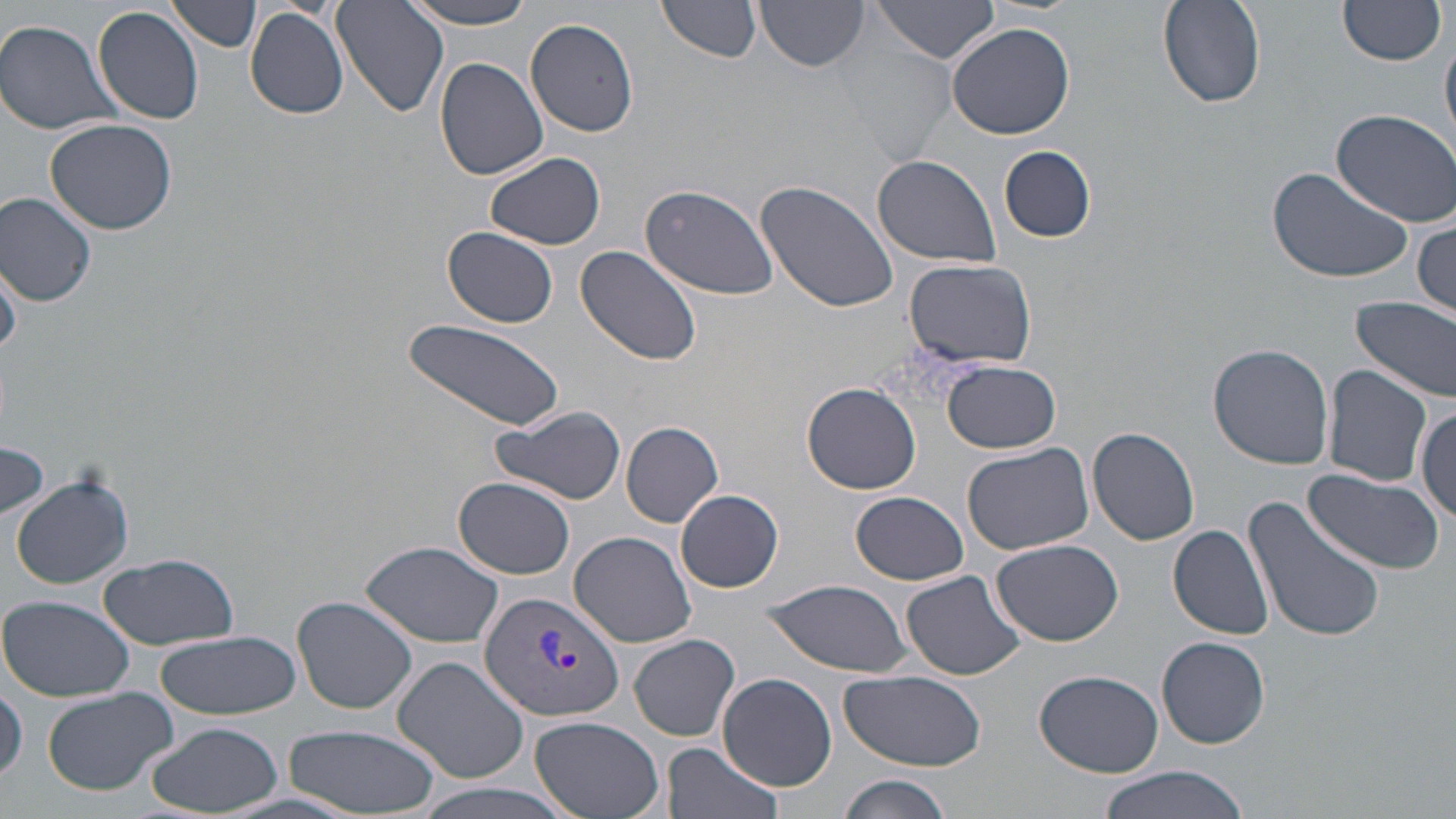

slide-level diagnosis = Plasmodium vivax
stain = May-Grünwald-Giemsa
field of view = single
preparation = thin blood film
magnification = 1000x
modality = optical microscopy
image size = 1456×819 pixels
uninfected red blood cell locations = approximate bounding boxes as [x1, y1, x2, y2] in pixels: [166, 0, 262, 52], [333, 0, 447, 117], [396, 0, 545, 28], [1156, 0, 1264, 108], [659, 1, 761, 63], [756, 1, 870, 74], [868, 1, 1002, 63], [1338, 2, 1446, 67], [94, 7, 207, 124], [244, 8, 350, 120], [524, 16, 639, 136], [0, 21, 124, 134], [946, 23, 1075, 140], [1441, 33, 1455, 149], [841, 48, 958, 163], [435, 57, 548, 180], [1329, 107, 1456, 226], [44, 118, 178, 237], [999, 146, 1097, 243], [484, 152, 607, 250], [873, 156, 1003, 269], [1265, 166, 1416, 285], [756, 181, 897, 316], [640, 182, 779, 302], [0, 193, 99, 307], [1414, 215, 1456, 318], [444, 226, 559, 327], [576, 246, 703, 366], [906, 258, 1037, 366], [0, 263, 24, 356], [1353, 296, 1456, 404], [399, 319, 566, 432], [1207, 343, 1334, 469], [943, 360, 1062, 453], [1322, 365, 1431, 486], [802, 381, 922, 494], [1414, 404, 1454, 523], [491, 406, 626, 506], [621, 421, 724, 528], [1088, 428, 1199, 546], [0, 440, 49, 523], [961, 440, 1098, 554], [1303, 470, 1446, 578], [11, 473, 133, 589], [452, 478, 575, 579], [676, 489, 783, 594], [852, 491, 968, 586], [1243, 497, 1387, 644], [1168, 525, 1276, 640], [568, 531, 697, 647], [361, 540, 504, 649], [990, 540, 1125, 646], [98, 552, 240, 647], [901, 570, 1026, 680], [762, 579, 916, 674], [292, 595, 418, 714], [1, 597, 135, 702], [155, 631, 300, 722], [628, 633, 740, 741], [1157, 636, 1271, 748], [393, 656, 528, 783], [839, 670, 986, 772], [1035, 670, 1166, 778], [717, 672, 837, 789], [1, 679, 26, 787], [42, 685, 183, 794], [529, 714, 667, 819], [140, 721, 282, 817], [283, 723, 441, 816], [663, 740, 783, 819], [1094, 767, 1258, 819], [839, 774, 954, 819], [414, 783, 575, 819]
Plasmodium vivax-infected red blood cell locations = approximate bounding boxes as [x1, y1, x2, y2] in pixels: [479, 591, 626, 721]